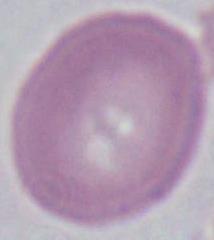 Photomicrograph. A red blood cell is shown. Captured at 1000x magnification.